Assess the morphology of the red blood cells.
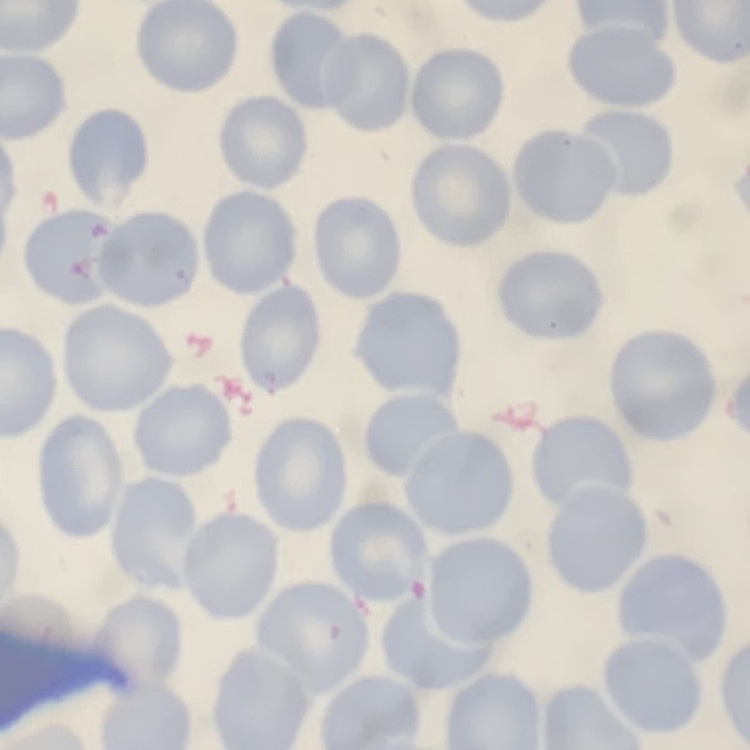
No rouleaux formation.

{
  "image_type": "one tile cut from a larger photomicrograph",
  "stain": "Field's or Giemsa",
  "preparation": "thin blood film"
}